Assess this cell for malaria.
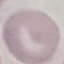

Uninfected.

Cell patch, automatically extracted from a larger field of view and resized to 64 × 64 pixels. Thin blood film. Giemsa-stained preparation. Photographed with a smartphone camera at the microscope eyepiece.